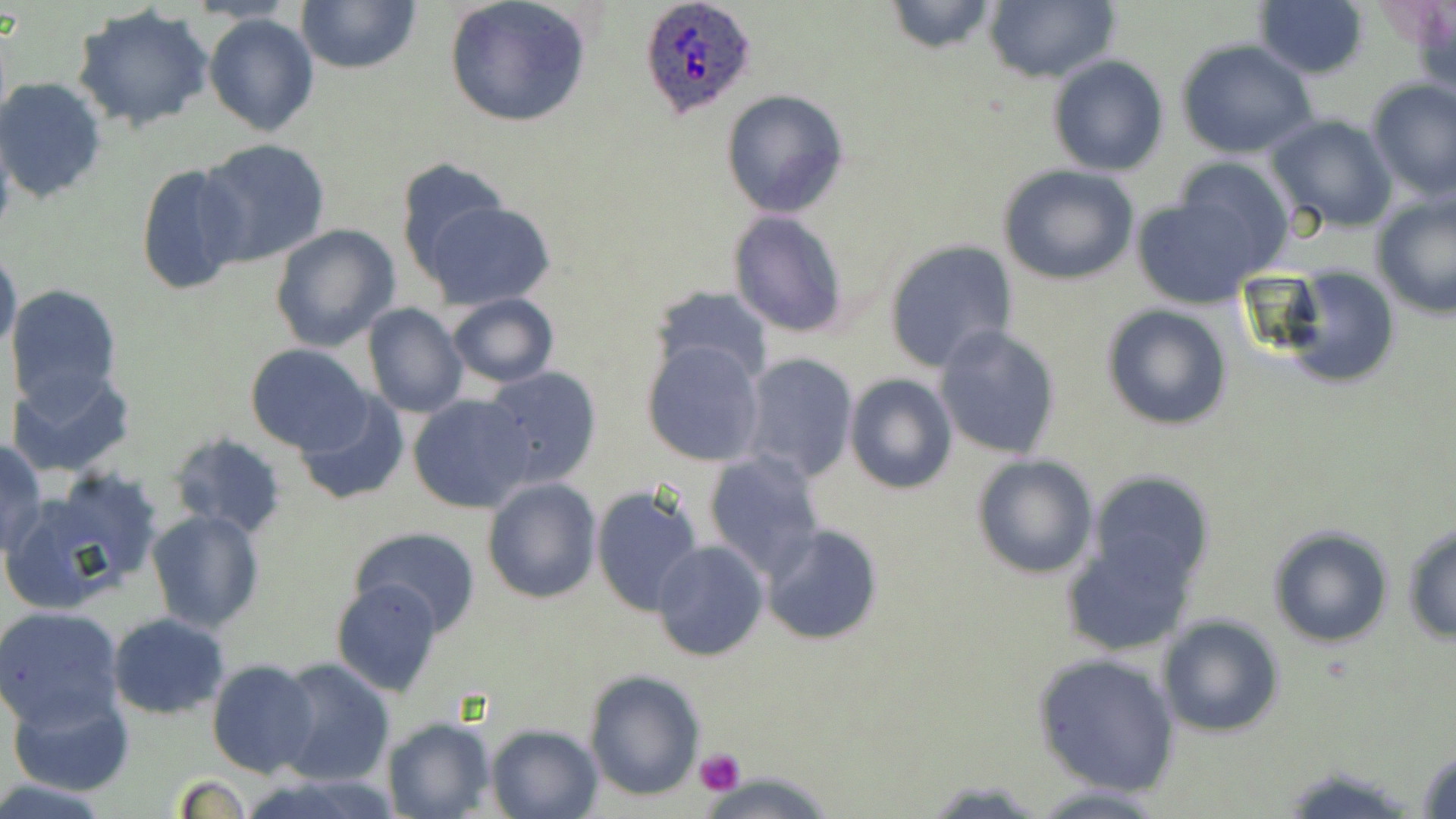

slide-level diagnosis = Plasmodium ovale
stain = May-Grünwald-Giemsa
Plasmodium ovale-infected red blood cell locations = approximate bounding boxes as (x1, y1, x2, y2) in pixels: (640, 0, 758, 120)
uninfected red blood cell locations = approximate bounding boxes as (x1, y1, x2, y2) in pixels: (188, 0, 299, 25), (295, 0, 421, 73), (443, 0, 593, 127), (982, 0, 1118, 85), (1252, 0, 1370, 79), (882, 1, 1000, 54), (71, 5, 216, 131), (204, 13, 319, 137), (1175, 39, 1319, 157), (1047, 56, 1169, 176), (0, 77, 107, 203), (1365, 80, 1456, 200), (721, 89, 849, 217), (1266, 114, 1398, 233), (198, 138, 331, 267), (1166, 156, 1293, 273), (396, 157, 513, 280), (134, 161, 253, 297), (997, 163, 1140, 286), (1371, 191, 1456, 319), (1130, 192, 1275, 307), (419, 199, 557, 311), (728, 210, 850, 338), (269, 223, 401, 353), (882, 239, 1020, 373), (0, 248, 21, 355), (1268, 264, 1402, 391), (5, 285, 123, 408), (650, 285, 776, 386), (445, 293, 558, 388), (1099, 302, 1234, 432), (363, 303, 469, 418), (934, 324, 1062, 462), (641, 339, 765, 467), (247, 344, 374, 453), (739, 353, 859, 483), (5, 365, 137, 479), (477, 365, 603, 490), (844, 373, 957, 496), (293, 392, 410, 504), (407, 394, 533, 514), (168, 432, 288, 538), (1, 437, 47, 557), (703, 450, 827, 578), (969, 454, 1099, 580), (1087, 470, 1215, 590), (481, 478, 602, 604), (7, 481, 156, 611), (591, 484, 705, 618), (146, 509, 265, 631), (759, 523, 885, 645), (1402, 523, 1456, 642), (1267, 524, 1396, 647), (352, 527, 481, 635), (1062, 531, 1198, 655), (651, 540, 771, 661), (332, 578, 446, 697), (0, 606, 125, 728), (107, 612, 229, 720), (1157, 614, 1286, 738), (1034, 652, 1179, 796), (275, 658, 396, 787), (207, 660, 320, 777), (585, 670, 705, 799), (7, 690, 133, 797), (382, 716, 496, 819), (485, 723, 605, 819), (1415, 745, 1456, 819), (1029, 783, 1177, 816)
modality = optical microscopy
platelet locations = approximate bounding boxes as (x1, y1, x2, y2) in pixels: (694, 748, 745, 795)
image size = 1456×819 pixels
preparation = thin blood smear
field of view = single
magnification = 1000x